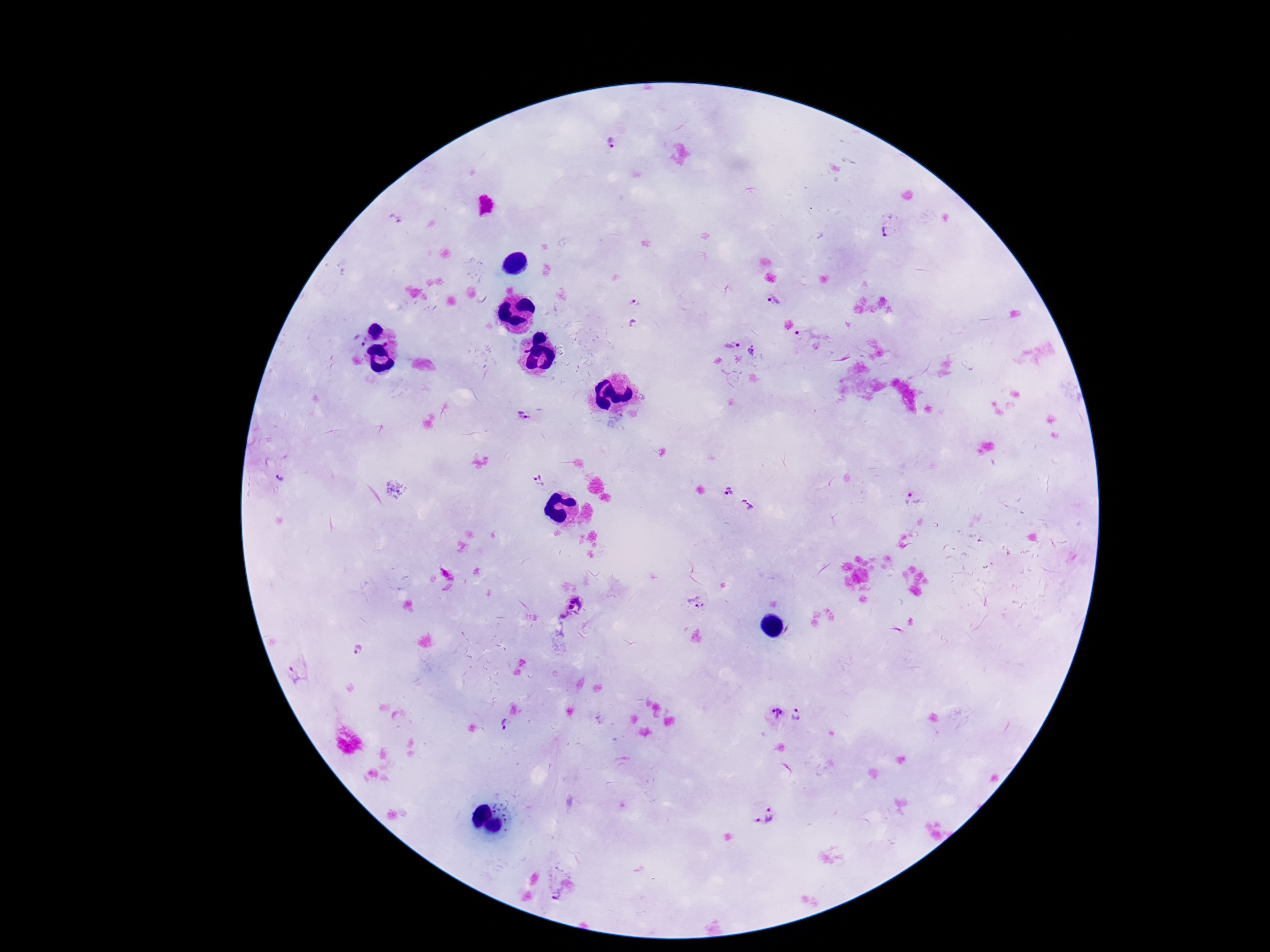

magnification = 100x
capture = smartphone camera through the microscope eyepiece
patient malaria status = positive
field of view = one from this slide
stain = Giemsa
Plasmodium parasite locations = approximate centers as {x, y} in pixels: {614, 147}, {395, 220}, {889, 228}, {775, 300}, {634, 301}, {802, 334}, {358, 340}, {731, 344}, {753, 352}, {526, 416}, {280, 478}, {537, 480}, {728, 491}, {913, 500}, {747, 505}, {696, 601}, {569, 607}, {358, 650}, {300, 671}, {775, 714}, {798, 715}, {504, 728}, {763, 815}
image size = 1270×952 pixels
preparation = thick blood smear